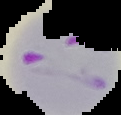
Summary:
  - Image type: cell region segmented out of the field of view; surrounding area masked to black
  - Result: Plasmodium parasites detected
  - Image size: 121×115 pixels
  - Preparation: thin blood smear